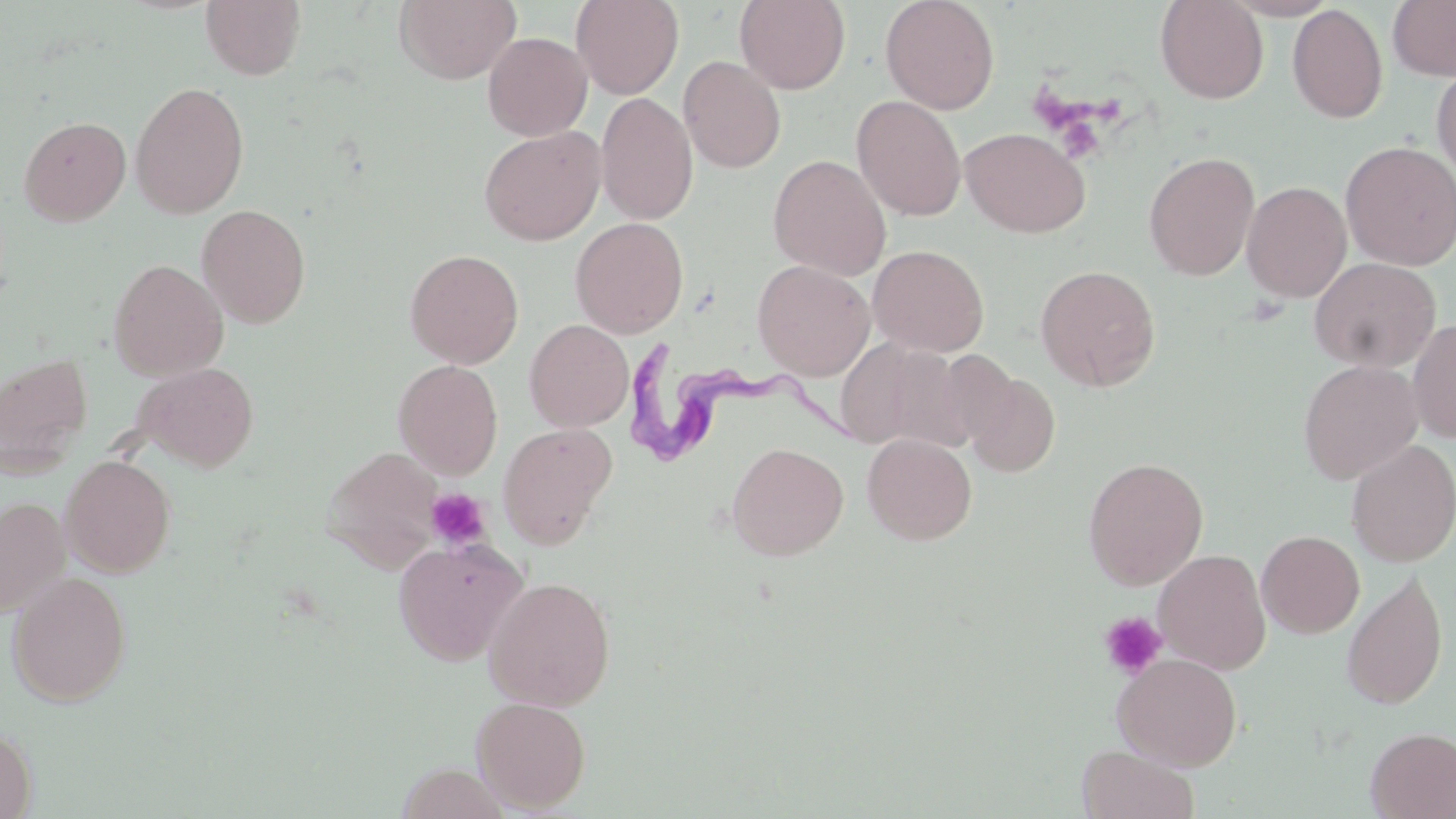

Summary:
  - Coordinate format: approximate bounding boxes as (x1,y1)-(x2,y2) corner pairs in pixels
  - Platelet locations: (425,488)-(491,551), (1099,612)-(1168,680)
  - Trypanosoma brucei locations: (611,337)-(882,467)
  - Uninfected red blood cell locations: (201,0)-(307,80), (394,0)-(521,84), (571,0)-(684,99), (734,0)-(851,93), (880,0)-(1000,114), (1155,0)-(1269,103), (1388,0)-(1456,81), (1287,4)-(1388,123), (483,32)-(592,140), (678,56)-(786,174), (1431,60)-(1456,181), (130,81)-(249,219), (596,92)-(698,226), (851,95)-(967,221), (18,115)-(131,226), (478,125)-(606,245), (960,127)-(1090,237), (1339,140)-(1456,270), (1143,151)-(1259,281), (768,154)-(891,280), (1242,180)-(1352,303), (197,204)-(312,327), (570,217)-(689,338), (868,244)-(989,356), (405,249)-(524,369), (1310,257)-(1441,373), (108,259)-(228,380), (752,260)-(875,380), (1035,264)-(1161,392), (1408,318)-(1456,444), (524,320)-(633,431), (835,337)-(970,451), (933,349)-(1019,449), (1,353)-(93,477), (392,359)-(503,480), (1298,360)-(1423,485), (134,362)-(258,472), (963,370)-(1060,478), (497,422)-(617,549), (862,433)-(978,545), (1346,439)-(1456,567), (727,442)-(848,560), (324,446)-(444,571), (60,455)-(176,577), (1083,457)-(1208,590), (0,496)-(70,618), (1256,530)-(1364,638), (393,536)-(527,666), (1153,549)-(1271,674), (7,571)-(132,707), (1341,571)-(1448,710), (482,576)-(616,711), (1112,653)-(1243,770), (471,696)-(591,812), (0,724)-(36,819), (1365,727)-(1456,819), (1077,745)-(1200,819)
  - Slide-level diagnosis: Trypanosoma brucei
  - Magnification: 1000x
  - Field of view: one of a larger specimen
  - Stain: May-Grünwald-Giemsa
  - Image size: 1456×819 pixels
  - Modality: optical microscopy
  - Preparation: thin blood film